State the preparation type.
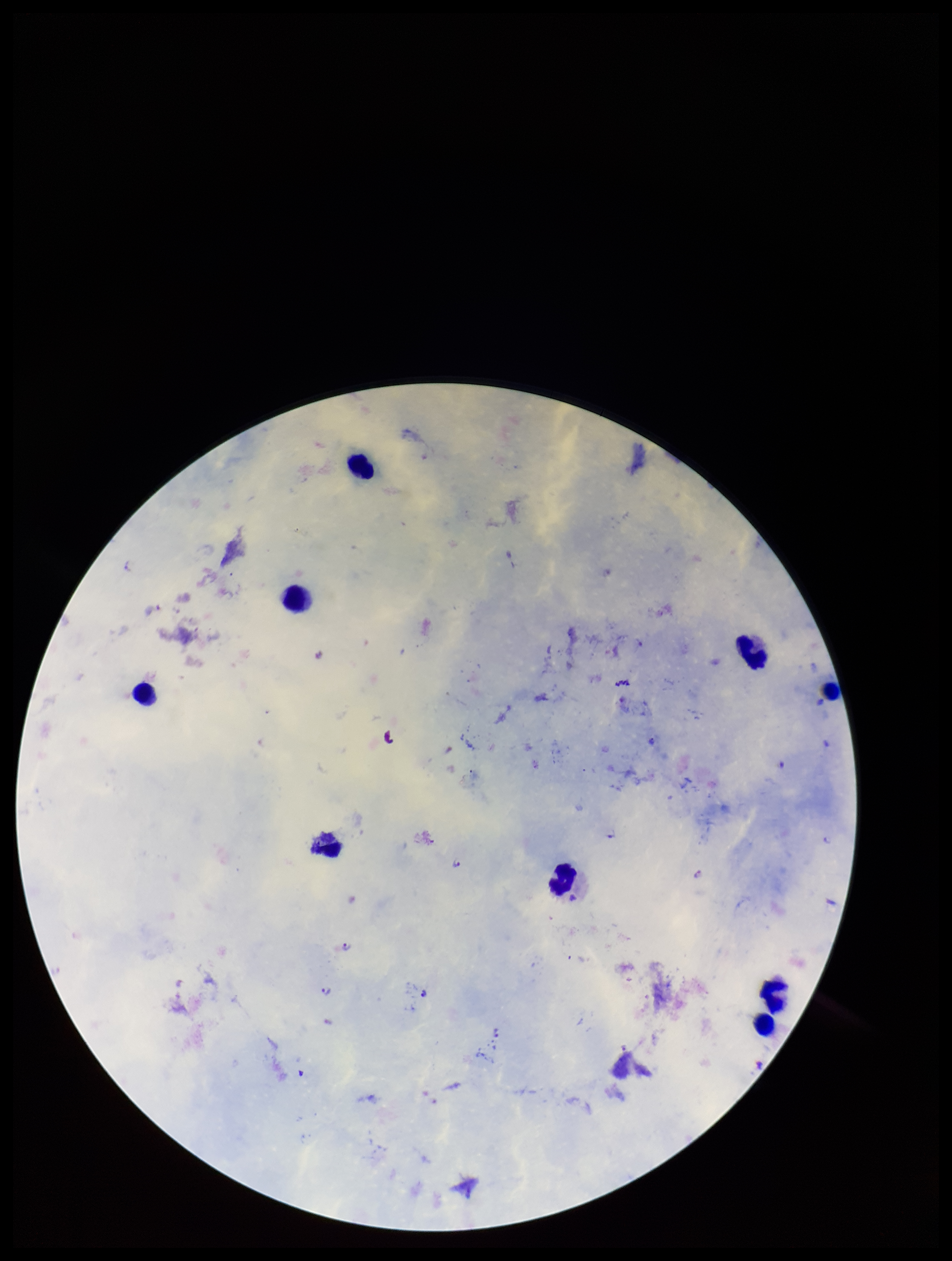
A thick smear.

Summary:
  - Leukocyte count: 9
  - Stain: Giemsa
  - Field of view: single
  - Image size: 952×1261 pixels
  - Plasmodium parasites: detected
  - Species reported for this patient: Plasmodium falciparum
  - Parasite count: 8
  - Patient malaria status: positive
  - Capture: smartphone photograph through the microscope eyepiece